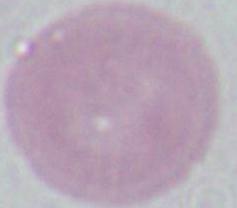 A red blood cell is seen. Micrograph. 1000x magnification.